Assess the morphology of the red blood cells.
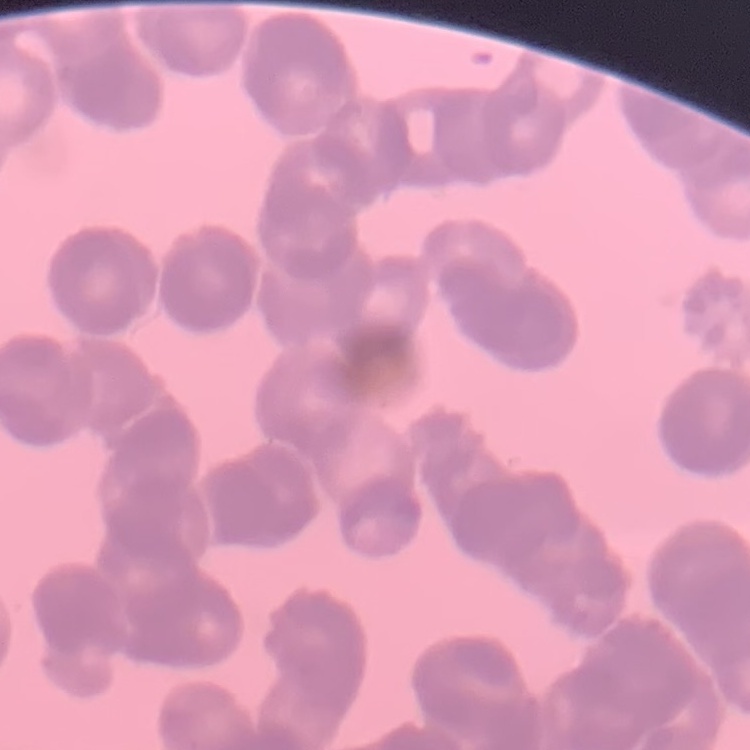

Rouleaux formation.

Thin blood film. Square crop of a larger photomicrograph. Stained with either Field's or Giemsa.